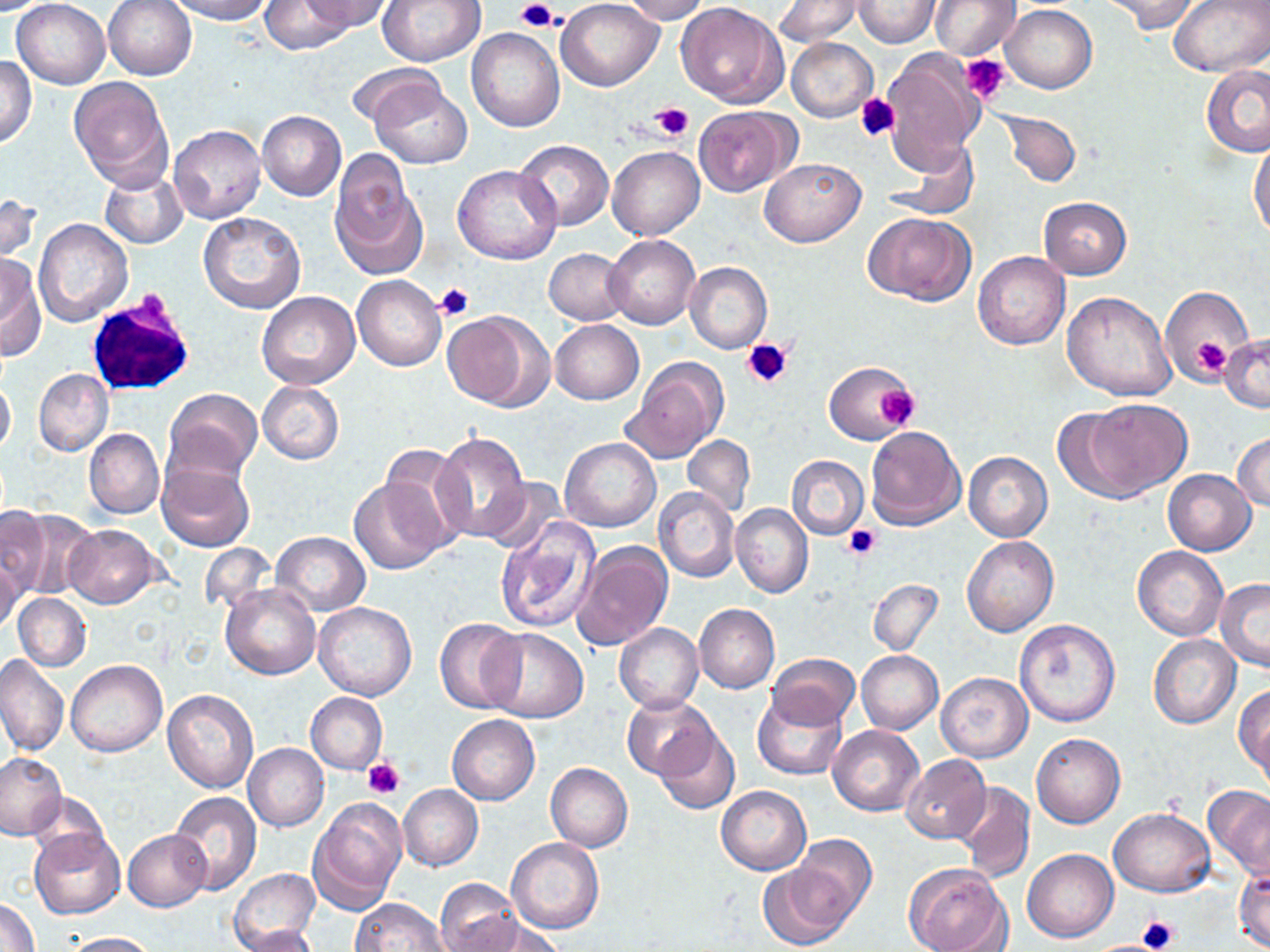
Approximate bounding boxes as named x1/y1/x2/y2 corners in pixels. Platelet locations: (x1=515, y1=1, x2=560, y2=32), (x1=961, y1=54, x2=1011, y2=105), (x1=855, y1=94, x2=900, y2=143), (x1=650, y1=102, x2=692, y2=141), (x1=434, y1=282, x2=474, y2=321), (x1=743, y1=335, x2=795, y2=388), (x1=1191, y1=336, x2=1233, y2=377), (x1=879, y1=384, x2=920, y2=429), (x1=844, y1=524, x2=882, y2=561), (x1=363, y1=755, x2=405, y2=798), (x1=1139, y1=914, x2=1179, y2=950). White blood cell locations: (x1=86, y1=293, x2=197, y2=396). Uninfected red blood cell locations: (x1=11, y1=0, x2=110, y2=88), (x1=102, y1=0, x2=198, y2=80), (x1=165, y1=0, x2=271, y2=23), (x1=261, y1=0, x2=353, y2=54), (x1=301, y1=0, x2=394, y2=33), (x1=377, y1=0, x2=486, y2=67), (x1=555, y1=0, x2=664, y2=90), (x1=616, y1=0, x2=711, y2=23), (x1=929, y1=0, x2=1020, y2=60), (x1=1100, y1=0, x2=1201, y2=35), (x1=1169, y1=0, x2=1268, y2=76), (x1=0, y1=1, x2=57, y2=15), (x1=774, y1=1, x2=862, y2=46), (x1=851, y1=1, x2=941, y2=48), (x1=677, y1=3, x2=789, y2=109), (x1=1001, y1=4, x2=1096, y2=93), (x1=466, y1=28, x2=564, y2=133), (x1=786, y1=37, x2=877, y2=122), (x1=882, y1=49, x2=985, y2=169), (x1=0, y1=53, x2=36, y2=148), (x1=348, y1=62, x2=448, y2=139), (x1=1201, y1=63, x2=1270, y2=158), (x1=68, y1=76, x2=173, y2=186), (x1=367, y1=78, x2=473, y2=169), (x1=695, y1=106, x2=797, y2=195), (x1=257, y1=110, x2=347, y2=201), (x1=996, y1=110, x2=1082, y2=187), (x1=169, y1=124, x2=265, y2=224), (x1=1249, y1=136, x2=1270, y2=243), (x1=887, y1=137, x2=976, y2=219), (x1=515, y1=139, x2=614, y2=230), (x1=607, y1=146, x2=704, y2=241), (x1=759, y1=157, x2=865, y2=247), (x1=329, y1=158, x2=425, y2=280), (x1=451, y1=166, x2=561, y2=265), (x1=99, y1=169, x2=188, y2=248), (x1=0, y1=191, x2=40, y2=266), (x1=1037, y1=198, x2=1131, y2=280), (x1=863, y1=211, x2=976, y2=306), (x1=197, y1=212, x2=304, y2=315), (x1=33, y1=219, x2=133, y2=327), (x1=605, y1=234, x2=701, y2=330), (x1=544, y1=247, x2=631, y2=324), (x1=972, y1=252, x2=1070, y2=350), (x1=0, y1=255, x2=45, y2=361), (x1=684, y1=262, x2=771, y2=353), (x1=352, y1=275, x2=446, y2=370), (x1=1160, y1=286, x2=1252, y2=380), (x1=1062, y1=289, x2=1177, y2=400), (x1=257, y1=292, x2=360, y2=389), (x1=444, y1=308, x2=550, y2=410), (x1=550, y1=319, x2=644, y2=404), (x1=1219, y1=334, x2=1270, y2=413), (x1=624, y1=359, x2=727, y2=462), (x1=825, y1=360, x2=917, y2=445), (x1=33, y1=369, x2=113, y2=456), (x1=0, y1=377, x2=15, y2=457), (x1=257, y1=381, x2=344, y2=464), (x1=164, y1=388, x2=263, y2=484), (x1=1072, y1=400, x2=1191, y2=499), (x1=865, y1=426, x2=966, y2=531), (x1=83, y1=428, x2=163, y2=518), (x1=432, y1=430, x2=531, y2=545), (x1=1232, y1=432, x2=1270, y2=511), (x1=682, y1=436, x2=754, y2=515), (x1=560, y1=437, x2=660, y2=533), (x1=379, y1=444, x2=471, y2=553), (x1=964, y1=452, x2=1053, y2=542), (x1=788, y1=454, x2=868, y2=539), (x1=157, y1=461, x2=254, y2=552), (x1=1162, y1=469, x2=1256, y2=555), (x1=350, y1=476, x2=453, y2=574), (x1=481, y1=476, x2=568, y2=556), (x1=654, y1=487, x2=740, y2=583), (x1=730, y1=504, x2=813, y2=598), (x1=0, y1=505, x2=50, y2=600), (x1=11, y1=509, x2=97, y2=600), (x1=494, y1=519, x2=601, y2=634), (x1=64, y1=524, x2=163, y2=609), (x1=271, y1=531, x2=370, y2=616), (x1=962, y1=535, x2=1058, y2=636), (x1=571, y1=539, x2=674, y2=650), (x1=199, y1=544, x2=276, y2=617), (x1=1132, y1=545, x2=1228, y2=640), (x1=0, y1=555, x2=22, y2=637), (x1=867, y1=578, x2=943, y2=656), (x1=1215, y1=578, x2=1270, y2=672), (x1=221, y1=583, x2=320, y2=679), (x1=14, y1=593, x2=91, y2=671), (x1=314, y1=601, x2=417, y2=701), (x1=694, y1=603, x2=779, y2=694), (x1=435, y1=617, x2=527, y2=713), (x1=1013, y1=618, x2=1122, y2=729), (x1=614, y1=623, x2=703, y2=713), (x1=483, y1=627, x2=589, y2=722), (x1=1149, y1=635, x2=1240, y2=729), (x1=856, y1=651, x2=943, y2=734), (x1=767, y1=653, x2=859, y2=730), (x1=0, y1=655, x2=68, y2=756), (x1=65, y1=659, x2=167, y2=757), (x1=935, y1=671, x2=1033, y2=762), (x1=1234, y1=683, x2=1270, y2=781), (x1=162, y1=688, x2=258, y2=794), (x1=752, y1=690, x2=847, y2=781), (x1=307, y1=693, x2=387, y2=773), (x1=622, y1=693, x2=718, y2=780), (x1=447, y1=715, x2=540, y2=805), (x1=829, y1=725, x2=924, y2=816), (x1=651, y1=726, x2=739, y2=816), (x1=1031, y1=732, x2=1125, y2=828), (x1=243, y1=743, x2=329, y2=832), (x1=0, y1=752, x2=65, y2=839), (x1=900, y1=754, x2=992, y2=843), (x1=546, y1=762, x2=633, y2=852), (x1=953, y1=783, x2=1035, y2=883), (x1=1203, y1=783, x2=1270, y2=882), (x1=398, y1=786, x2=482, y2=871), (x1=717, y1=786, x2=811, y2=875), (x1=27, y1=791, x2=110, y2=863), (x1=170, y1=793, x2=262, y2=894), (x1=309, y1=798, x2=406, y2=913), (x1=1109, y1=808, x2=1215, y2=897), (x1=29, y1=829, x2=125, y2=919), (x1=123, y1=829, x2=211, y2=912), (x1=790, y1=835, x2=877, y2=929), (x1=507, y1=837, x2=603, y2=933), (x1=1022, y1=848, x2=1118, y2=943), (x1=758, y1=863, x2=855, y2=948), (x1=905, y1=864, x2=1012, y2=952), (x1=1234, y1=865, x2=1270, y2=951), (x1=229, y1=868, x2=320, y2=952), (x1=435, y1=878, x2=523, y2=951), (x1=0, y1=895, x2=40, y2=951), (x1=349, y1=899, x2=452, y2=951), (x1=471, y1=916, x2=563, y2=952), (x1=240, y1=926, x2=321, y2=952), (x1=57, y1=931, x2=155, y2=951). Slide-level diagnosis: no evidence of blood parasites. May-Grünwald-Giemsa-stained preparation. Image is 1270×952 pixels. Thin blood film. Captured at 1000x magnification. Optical microscopy. Single field of view.